Locate every blood parasite and identify its species.
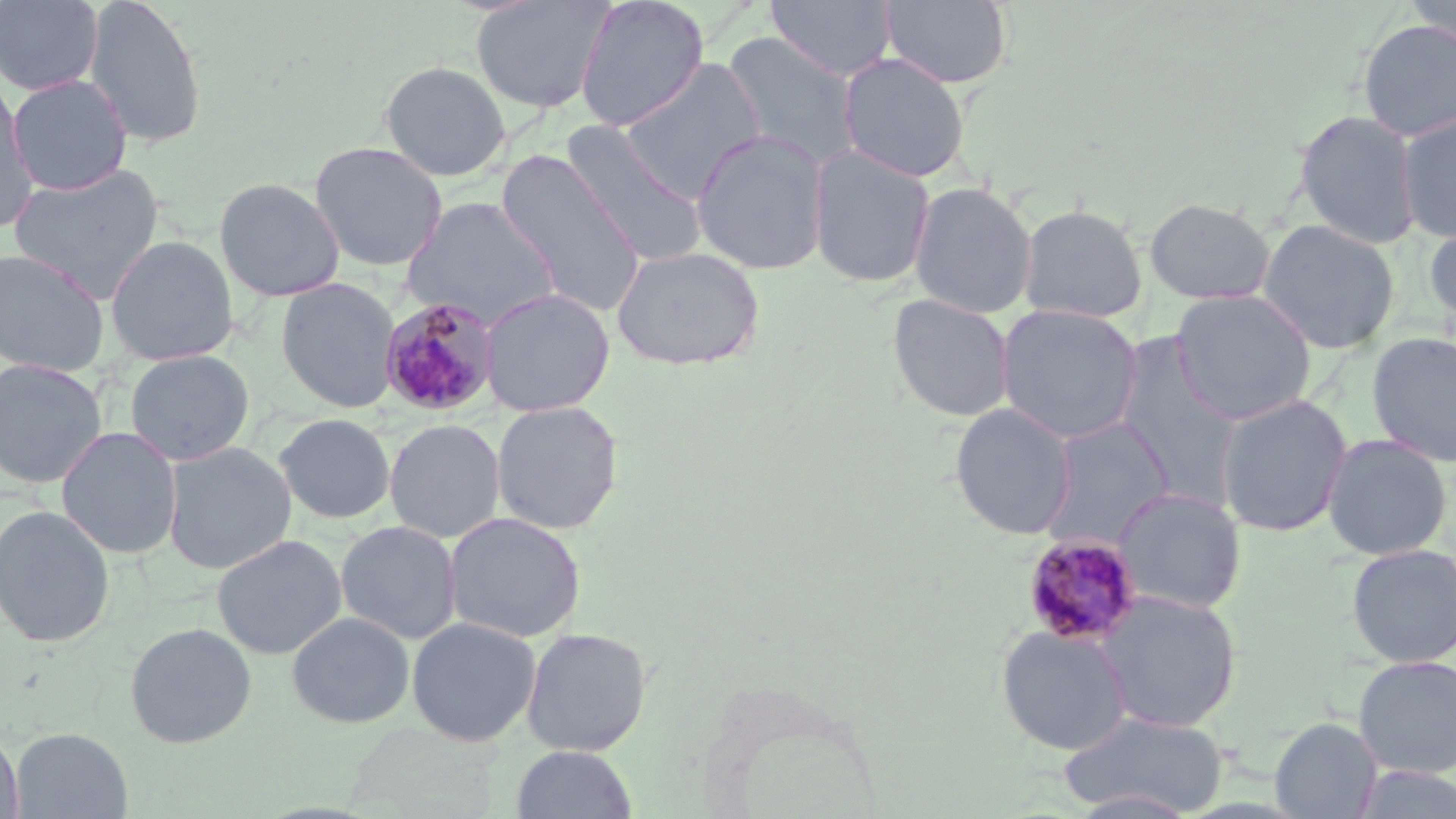
Approximate bounding boxes as [x1, y1, x2, y2] in pixels.
Plasmodium malariae-infected red blood cells: [379, 297, 501, 417], [1022, 533, 1143, 646].
No Plasmodium falciparum, Plasmodium ovale, Plasmodium vivax, Babesia divergens, or Trypanosoma brucei observed.

slide-level diagnosis = Plasmodium malariae
image size = 1456×819 pixels
field of view = one of a larger specimen
magnification = 1000x
preparation = thin blood film
modality = light microscopy
uninfected red blood cell locations = approximate bounding boxes as [x1, y1, x2, y2] in pixels: [82, 0, 209, 149], [470, 0, 617, 114], [574, 0, 710, 132], [765, 0, 897, 82], [879, 0, 1014, 89], [1405, 0, 1455, 49], [0, 1, 103, 96], [1357, 19, 1456, 143], [721, 31, 863, 170], [837, 53, 970, 183], [618, 57, 767, 200], [379, 60, 511, 181], [6, 74, 132, 195], [0, 80, 40, 230], [1293, 109, 1422, 250], [1395, 111, 1456, 244], [561, 121, 708, 266], [690, 128, 831, 276], [309, 141, 448, 272], [807, 145, 936, 288], [495, 150, 647, 317], [8, 162, 165, 302], [214, 177, 345, 302], [908, 180, 1038, 319], [401, 196, 562, 330], [1144, 197, 1277, 305], [1017, 204, 1148, 323], [1423, 218, 1456, 337], [1257, 219, 1400, 355], [105, 235, 239, 365], [611, 245, 765, 371], [0, 248, 111, 376], [275, 276, 402, 413], [479, 287, 615, 417], [1169, 289, 1318, 425], [887, 293, 1016, 423], [995, 304, 1143, 446], [1366, 330, 1456, 468], [1112, 332, 1246, 507], [125, 349, 254, 466], [0, 358, 108, 489], [1214, 393, 1353, 538], [490, 400, 625, 535], [949, 403, 1078, 540], [273, 413, 396, 524], [1037, 417, 1176, 552], [384, 419, 506, 543], [56, 426, 182, 559], [1321, 433, 1453, 560], [161, 441, 297, 575], [1114, 487, 1247, 614], [0, 503, 116, 649], [443, 511, 587, 643], [335, 520, 462, 645], [211, 533, 347, 659], [1345, 543, 1456, 668], [1093, 591, 1243, 734], [286, 612, 415, 728], [406, 615, 541, 747], [124, 622, 257, 748], [996, 624, 1132, 755], [520, 627, 652, 756], [1352, 654, 1456, 779], [1057, 710, 1229, 817], [1269, 716, 1382, 818], [0, 727, 23, 819], [11, 727, 132, 818], [510, 745, 638, 819], [1349, 764, 1456, 819]
stain = May-Grünwald-Giemsa